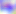

400x magnification. Toxoplasma gondii is shown. Photomicrograph.